Classify this cell by malaria status.
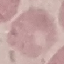

It is uninfected.

{
  "image_type": "cell patch, automatically extracted from a larger field of view and resized to 64 × 64 pixels",
  "preparation": "thin smear",
  "capture": "smartphone camera at the microscope eyepiece",
  "stain": "Giemsa"
}